Describe the morphology of the red blood cells.
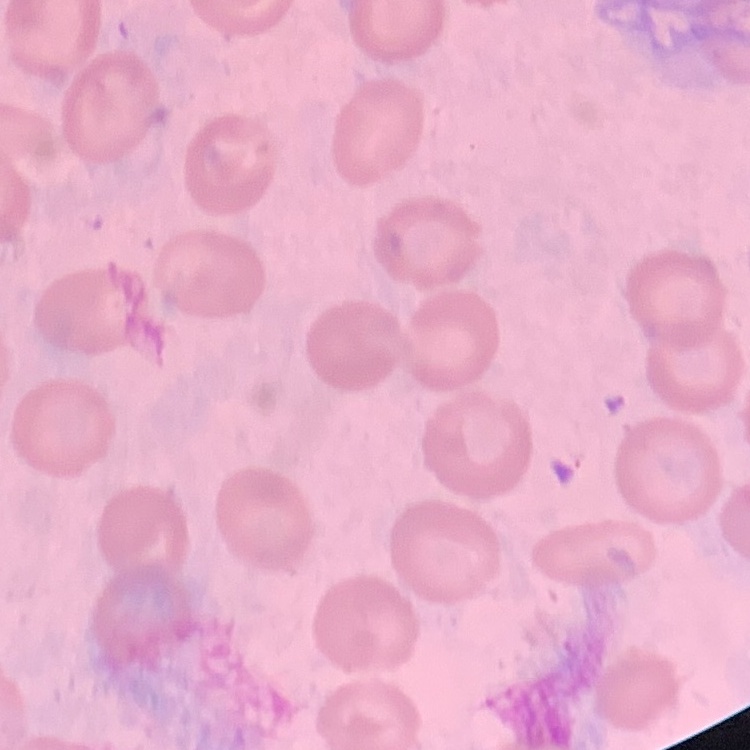

They show no rouleaux formation.

image type = square crop of a larger photomicrograph
preparation = thin peripheral smear
stain = Field's or Giemsa